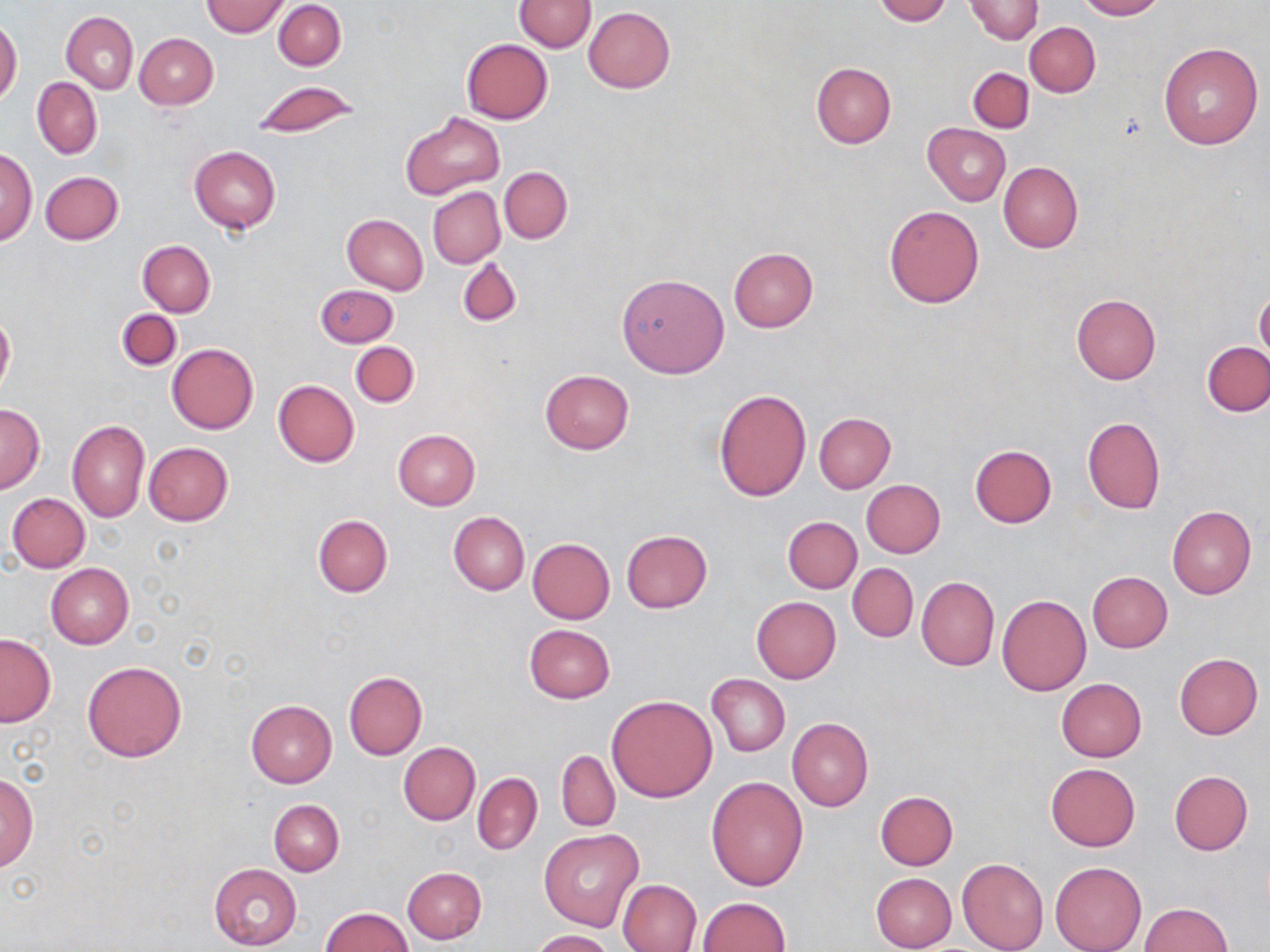
slide-level diagnosis = negative for blood parasites
preparation = thin blood smear
image size = 1270×952 pixels
modality = optical microscopy
field of view = one of a larger specimen
magnification = 1000x
uninfected red blood cell locations = approximate bounding boxes as [x1, y1, x2, y2] in pixels: [203, 0, 289, 38], [873, 0, 950, 24], [965, 0, 1043, 43], [1073, 0, 1163, 20], [274, 1, 346, 71], [514, 1, 595, 52], [584, 7, 676, 93], [62, 11, 138, 93], [0, 19, 22, 105], [1025, 22, 1099, 97], [135, 33, 218, 110], [461, 39, 552, 123], [1158, 42, 1264, 148], [810, 63, 896, 149], [968, 67, 1034, 133], [32, 77, 102, 159], [251, 81, 357, 140], [401, 112, 504, 199], [922, 123, 1010, 206], [189, 146, 281, 233], [1, 147, 36, 246], [998, 161, 1083, 253], [500, 166, 571, 243], [41, 171, 124, 245], [428, 187, 505, 269], [885, 205, 984, 308], [341, 214, 428, 295], [138, 240, 215, 316], [729, 247, 818, 331], [456, 256, 522, 326], [616, 272, 730, 378], [315, 285, 398, 347], [1255, 289, 1269, 365], [1071, 294, 1161, 384], [115, 309, 182, 371], [0, 314, 15, 392], [350, 341, 420, 408], [1203, 341, 1269, 416], [167, 343, 258, 433], [540, 369, 635, 454], [273, 380, 359, 467], [714, 389, 810, 501], [0, 404, 44, 492], [814, 413, 896, 493], [1082, 416, 1164, 514], [67, 419, 148, 522], [392, 429, 481, 510], [143, 443, 233, 526], [969, 445, 1057, 528], [861, 480, 945, 558], [8, 493, 90, 573], [1167, 505, 1256, 598], [448, 511, 530, 595], [313, 514, 392, 597], [782, 516, 861, 593], [622, 530, 711, 612], [528, 539, 615, 624], [848, 562, 918, 643], [46, 563, 134, 650], [1087, 572, 1173, 653], [916, 576, 999, 671], [997, 594, 1091, 696], [752, 596, 841, 684], [524, 624, 615, 703], [0, 633, 56, 727], [1174, 653, 1262, 739], [82, 661, 187, 762], [344, 671, 427, 759], [707, 673, 790, 757], [1056, 678, 1146, 761], [607, 695, 718, 802], [246, 699, 336, 786], [787, 717, 873, 812], [399, 742, 480, 825], [556, 750, 620, 831], [1046, 763, 1140, 851], [1, 770, 38, 871], [1169, 770, 1253, 854], [473, 773, 542, 854], [706, 776, 808, 890], [875, 790, 958, 870], [269, 800, 344, 875], [540, 830, 644, 932], [957, 857, 1048, 952], [1051, 861, 1146, 952], [208, 863, 301, 949], [402, 866, 486, 944], [870, 872, 957, 952], [617, 879, 702, 951], [696, 897, 789, 952], [1138, 903, 1232, 952], [320, 907, 414, 952], [532, 930, 613, 952]
stain = May-Grünwald-Giemsa